Report the malaria status of this cell.
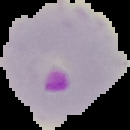

It is parasitized.

Summary:
  - Image size: 130×130 pixels
  - Preparation: thin blood film
  - Image type: cell region segmented out of the field of view; surrounding area masked to black